State which parasite is depicted.
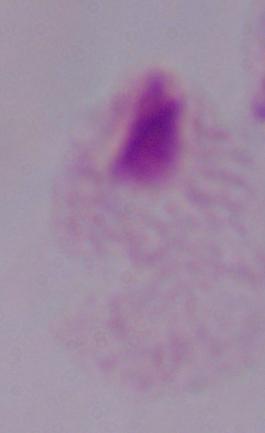

This is a trichomonad.

1000x magnification. Micrograph.